Classify this cell by malaria status.
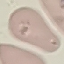

It is parasitized.

Summary:
  - Preparation: thin blood film
  - Capture: smartphone camera at the microscope eyepiece
  - Stain: Giemsa
  - Image type: automatically extracted cell patch, resized to 64 × 64 pixels